State which parasite is depicted.
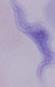
This is a trypanosome.

Photomicrograph. 1000x magnification.